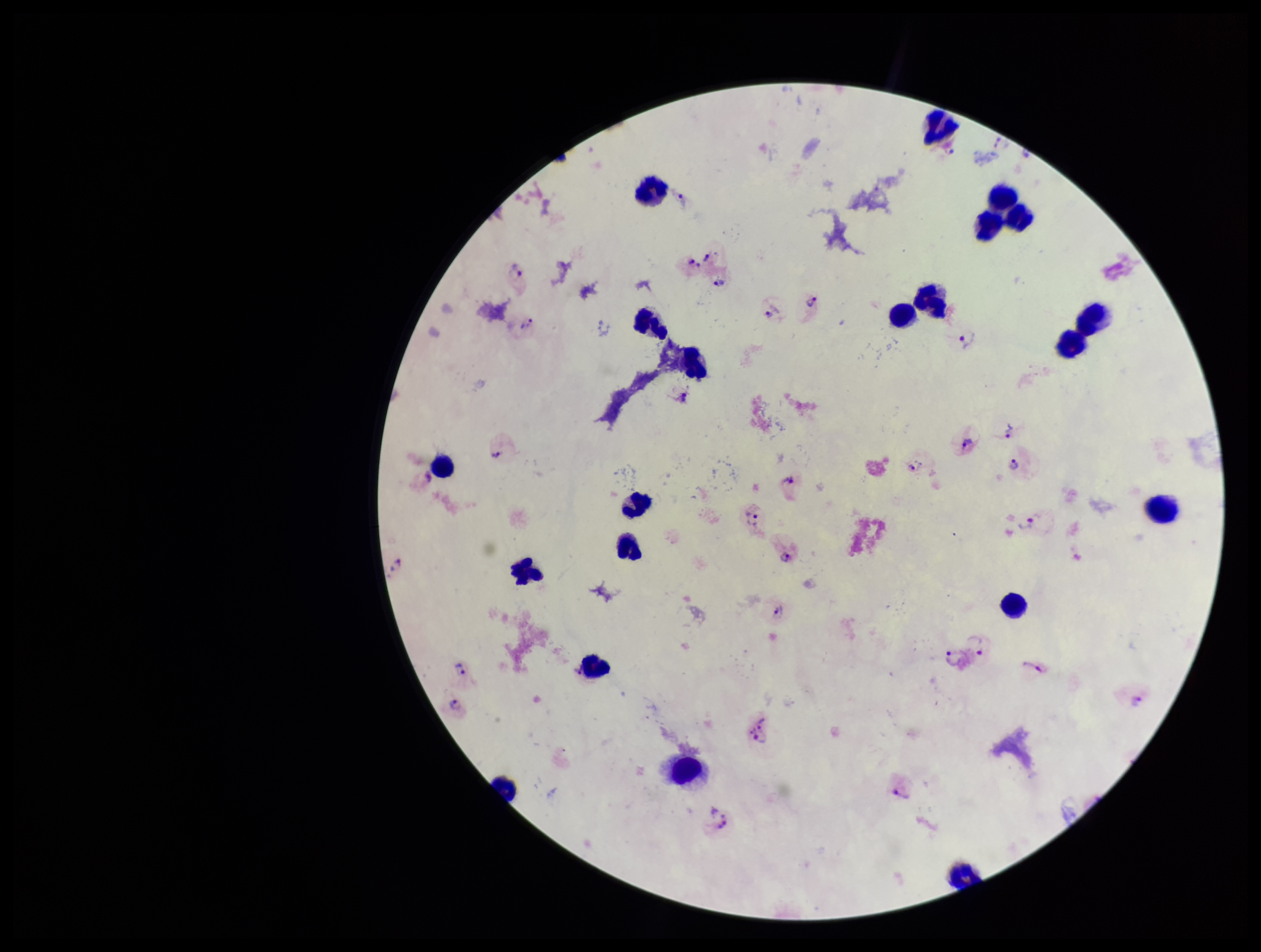
image size = 1261×952 pixels
Plasmodium parasites = detected
patient malaria status = infected
leukocyte count = 19
parasite count = 23
capture = smartphone photograph through the microscope eyepiece
field of view = one from this slide
stain = Giemsa
preparation = thick
species reported for this patient = Plasmodium vivax